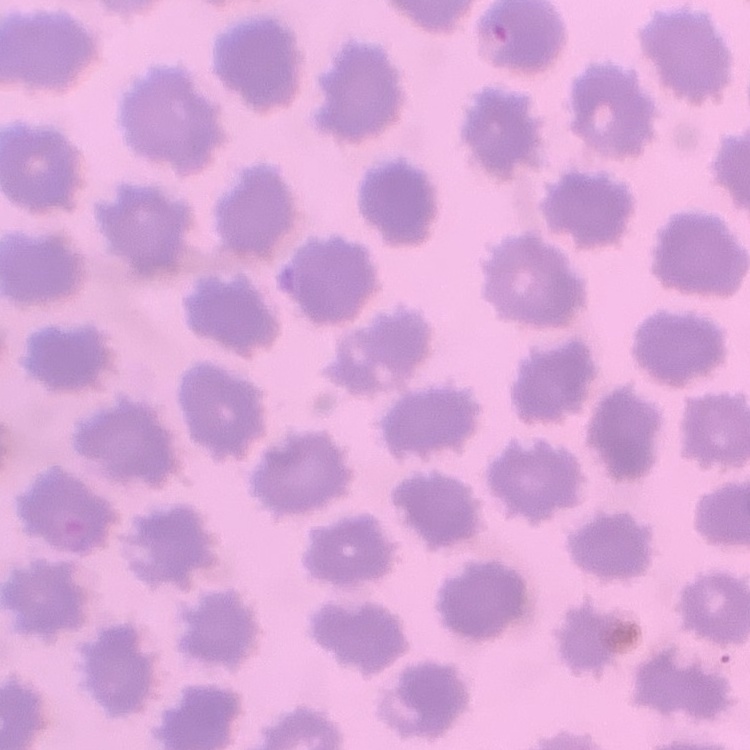
The red blood cells show no rouleaux formation. Square crop of a larger photomicrograph. Stained with either Field's or Giemsa. Thin blood smear.